Comment on the morphology of the erythrocytes.
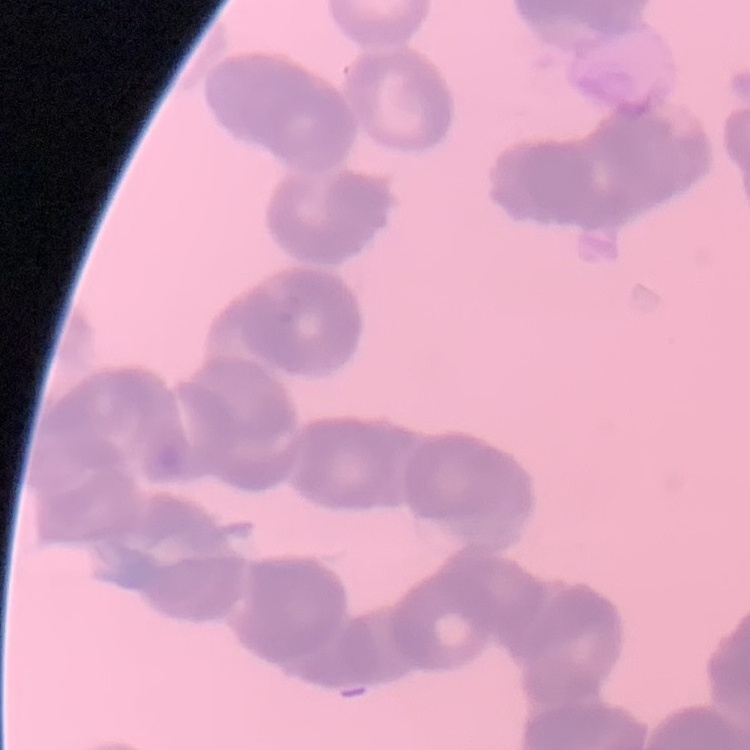

They show rouleaux formation.

One tile cut from a larger photomicrograph. Stained with either Field's or Giemsa. Thin peripheral smear.